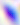
Summary:
  - Magnification: 400x
  - Identification: Toxoplasma gondii
  - Modality: photomicrograph